Locate platelets.
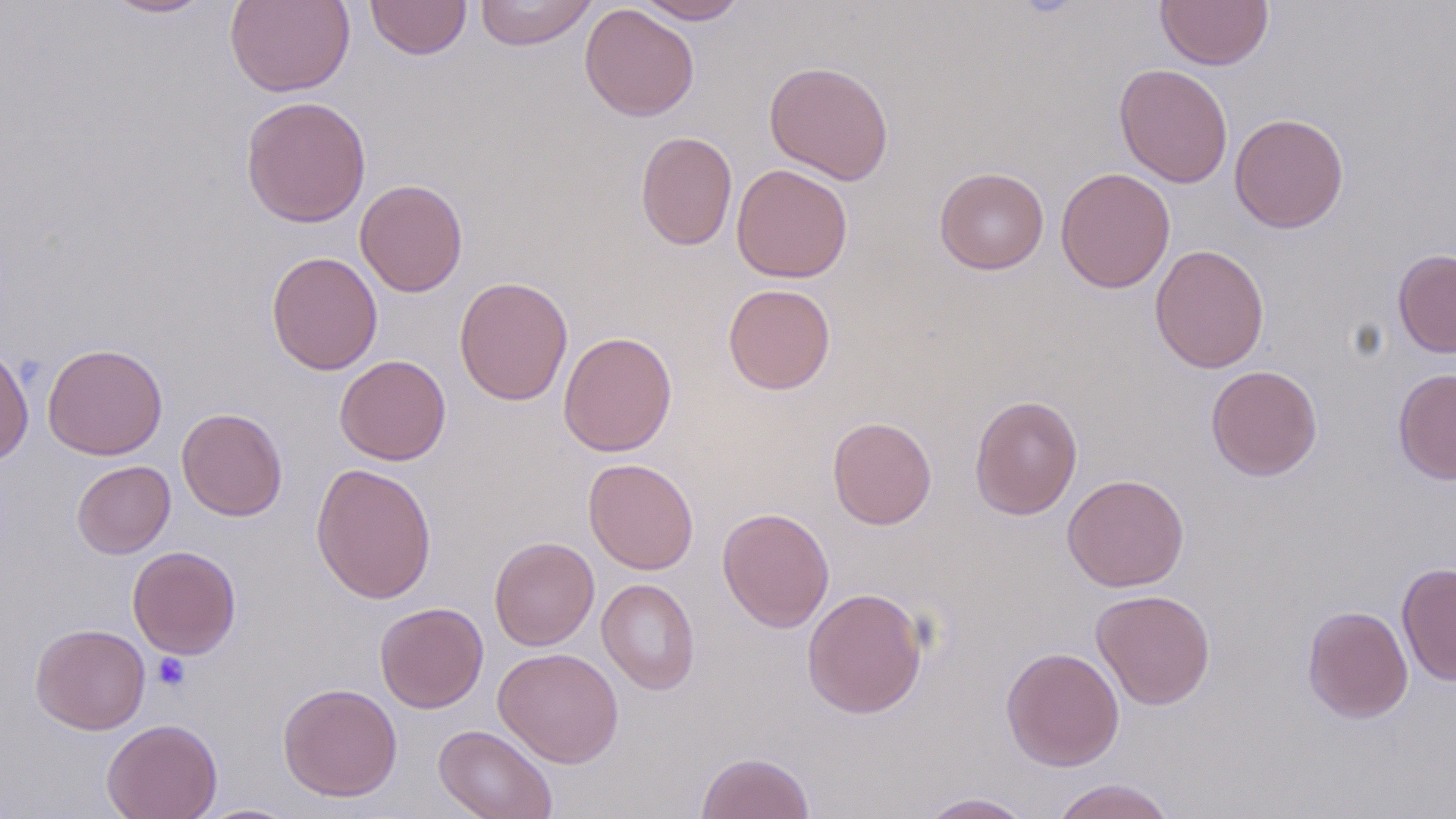

Approximate bounding boxes as named x1/y1/x2/y2 corners in pixels.
Platelets: (x1=152, y1=653, x2=191, y2=691).

Uninfected red blood cell locations: (x1=99, y1=0, x2=216, y2=19), (x1=225, y1=0, x2=356, y2=97), (x1=364, y1=0, x2=472, y2=60), (x1=634, y1=0, x2=749, y2=24), (x1=1156, y1=0, x2=1272, y2=70), (x1=474, y1=1, x2=598, y2=50), (x1=580, y1=3, x2=700, y2=122), (x1=764, y1=61, x2=895, y2=185), (x1=1114, y1=63, x2=1233, y2=188), (x1=240, y1=95, x2=372, y2=228), (x1=1228, y1=113, x2=1349, y2=233), (x1=635, y1=131, x2=738, y2=251), (x1=731, y1=164, x2=853, y2=283), (x1=934, y1=167, x2=1049, y2=274), (x1=1056, y1=167, x2=1175, y2=293), (x1=354, y1=178, x2=468, y2=297), (x1=1150, y1=244, x2=1270, y2=373), (x1=1393, y1=249, x2=1456, y2=358), (x1=266, y1=250, x2=383, y2=376), (x1=454, y1=276, x2=573, y2=406), (x1=723, y1=284, x2=836, y2=395), (x1=558, y1=331, x2=677, y2=457), (x1=42, y1=342, x2=168, y2=460), (x1=0, y1=344, x2=34, y2=467), (x1=335, y1=354, x2=451, y2=465), (x1=1206, y1=365, x2=1323, y2=481), (x1=1393, y1=367, x2=1456, y2=485), (x1=969, y1=394, x2=1083, y2=521), (x1=177, y1=407, x2=288, y2=521), (x1=827, y1=416, x2=937, y2=529), (x1=583, y1=458, x2=699, y2=575), (x1=71, y1=460, x2=175, y2=559), (x1=310, y1=462, x2=437, y2=603), (x1=1062, y1=473, x2=1189, y2=592), (x1=718, y1=507, x2=835, y2=633), (x1=489, y1=536, x2=599, y2=651), (x1=126, y1=545, x2=241, y2=659), (x1=1397, y1=561, x2=1455, y2=686), (x1=597, y1=578, x2=700, y2=695), (x1=802, y1=587, x2=928, y2=718), (x1=1091, y1=588, x2=1216, y2=710), (x1=374, y1=602, x2=488, y2=713), (x1=1302, y1=605, x2=1413, y2=723), (x1=30, y1=623, x2=151, y2=734), (x1=493, y1=647, x2=624, y2=768), (x1=1001, y1=647, x2=1125, y2=771), (x1=278, y1=682, x2=403, y2=802), (x1=102, y1=718, x2=222, y2=819), (x1=433, y1=723, x2=558, y2=819), (x1=695, y1=751, x2=815, y2=818), (x1=1050, y1=778, x2=1176, y2=819), (x1=914, y1=792, x2=1039, y2=819), (x1=192, y1=803, x2=304, y2=818). Slide-level diagnosis: no evidence of blood parasites. Thin blood film. Single field of view. 1000x magnification. Image is 1456×819 pixels. Light microscopy. May-Grünwald-Giemsa stain.